Report the malaria status of this cell.
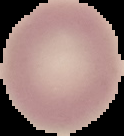
It is uninfected.

image size = 124×136 pixels
preparation = thin blood smear
image type = segmented cell region on a black background